Comment on the morphology of the red blood cells.
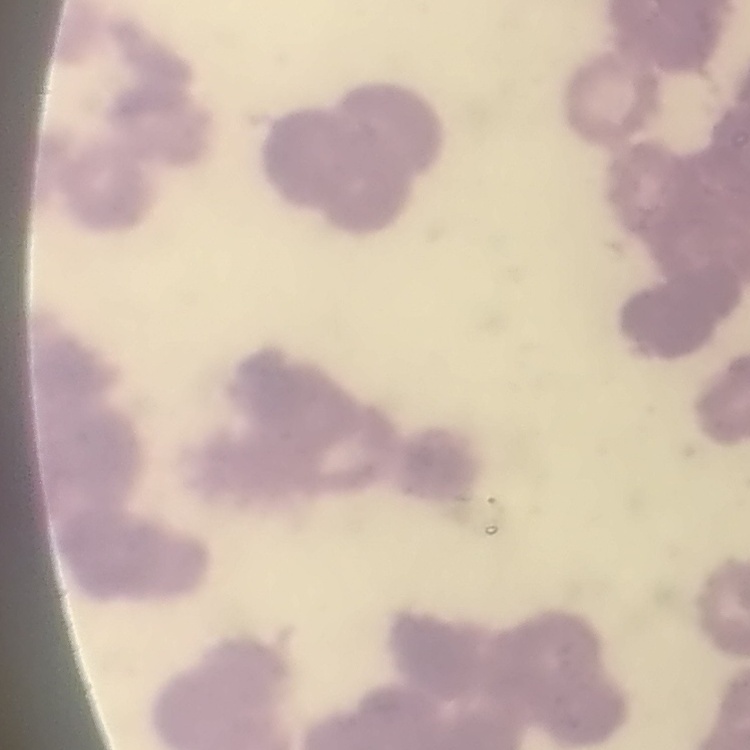

They show rouleaux formation.

stain = Field's or Giemsa
preparation = thin peripheral smear
image type = square crop of a larger photomicrograph